Assess this cell for malaria.
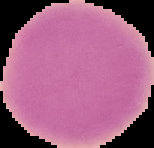
Uninfected.

Summary:
  - Preparation: thin blood smear
  - Image size: 154×148 pixels
  - Image type: segmented cell region on a black background